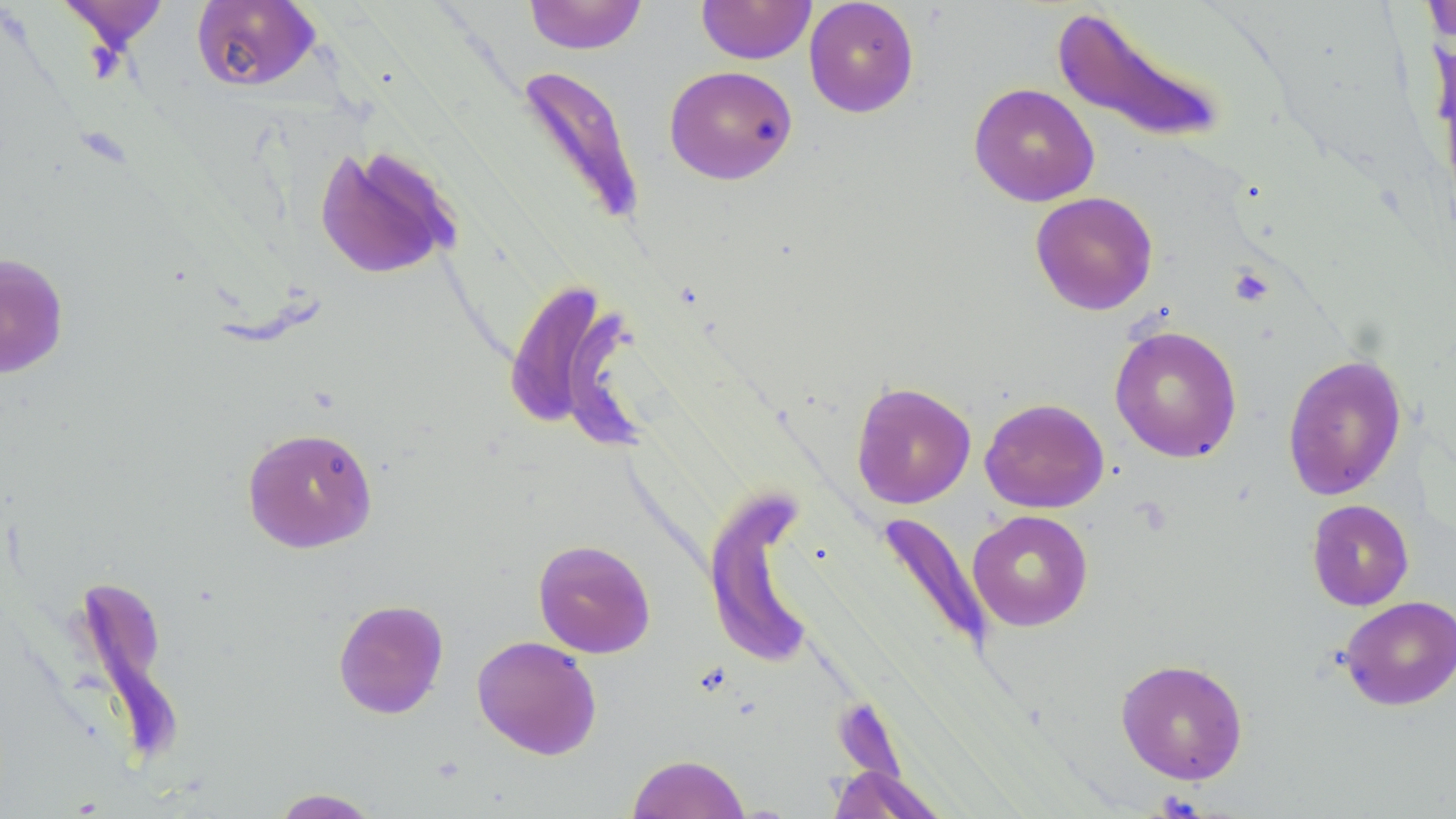
slide_level_diagnosis: no evidence of blood parasites
stain: May-Grünwald-Giemsa
image_size: 1456×819 pixels
preparation: thin blood film
modality: light microscopy
field_of_view: single
uninfected_red_blood_cell_locations: 'approximate bounding boxes as (x1,y1)-(x2,y2) corner pairs in pixels: (57,0)-(169,53), (523,0)-(648,55), (697,0)-(816,64), (804,0)-(920,117), (1421,0)-(1456,45), (191,1)-(320,92), (1051,5)-(1229,145), (515,64)-(646,227), (663,65)-(798,185), (968,83)-(1100,207), (312,144)-(464,281), (1030,191)-(1158,315), (0,252)-(70,379), (499,277)-(639,445), (1109,325)-(1243,463), (1283,354)-(1407,500), (851,381)-(976,509), (979,397)-(1109,514), (241,426)-(378,553), (704,488)-(815,669), (1307,499)-(1414,611), (967,509)-(1093,631), (875,511)-(994,655), (532,539)-(656,658), (72,571)-(180,759), (1339,595)-(1456,711), (332,598)-(449,719), (472,635)-(602,760), (1115,658)-(1249,784), (627,753)-(751,818), (827,764)-(949,818), (269,788)-(384,818)'
magnification: 1000x
platelet_locations: 'approximate bounding boxes as (x1,y1)-(x2,y2) corner pairs in pixels: (1230,267)-(1274,306)'